Give the extent of all uninfected red blood cells.
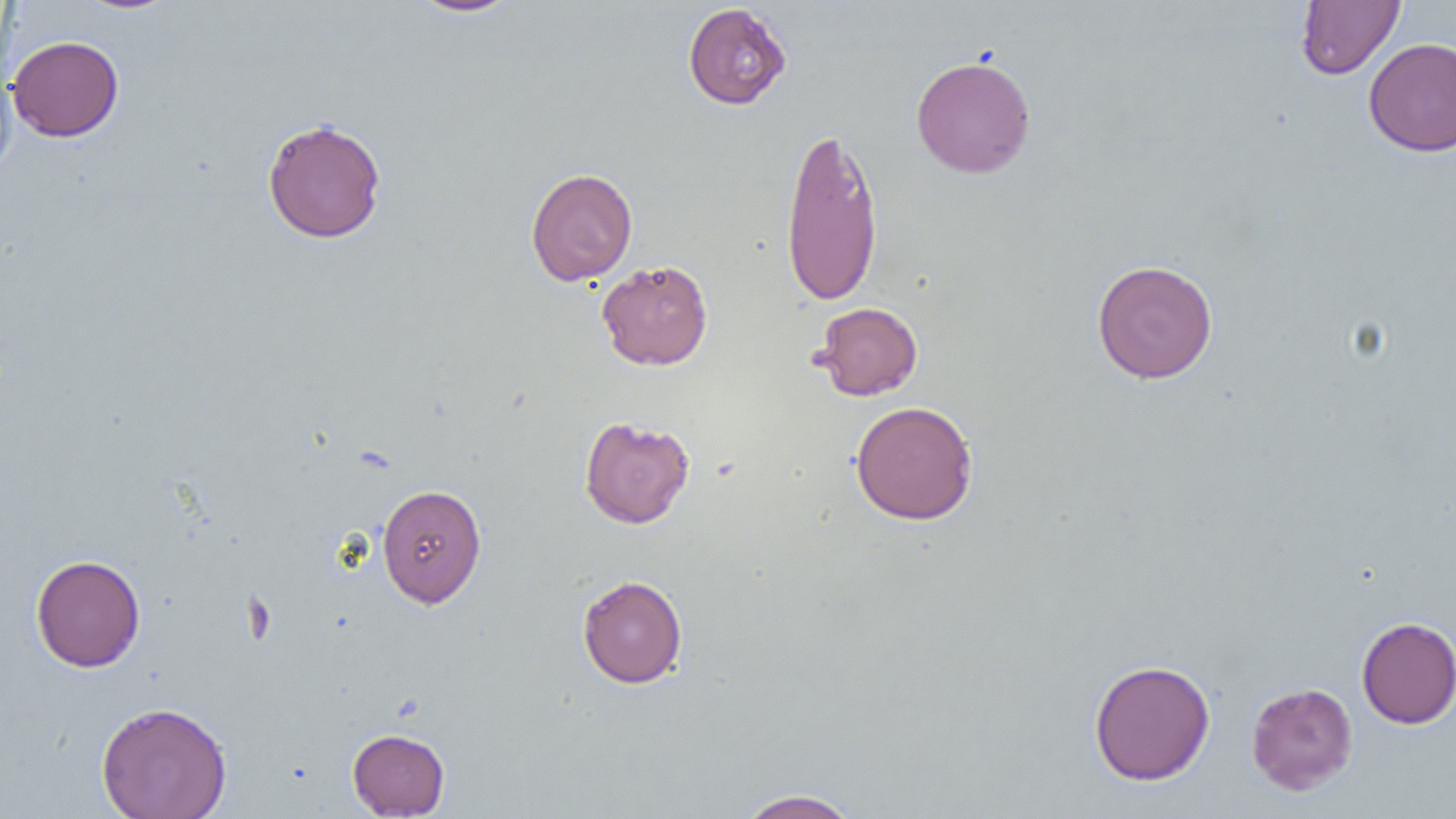
Approximate bounding boxes as named x1/y1/x2/y2 corners in pixels.
Uninfected red blood cells: (x1=76, y1=0, x2=181, y2=15), (x1=408, y1=0, x2=522, y2=17), (x1=1295, y1=1, x2=1406, y2=79), (x1=682, y1=3, x2=792, y2=110), (x1=7, y1=35, x2=124, y2=142), (x1=1363, y1=37, x2=1456, y2=156), (x1=910, y1=54, x2=1036, y2=179), (x1=0, y1=66, x2=18, y2=181), (x1=262, y1=117, x2=387, y2=244), (x1=779, y1=123, x2=884, y2=307), (x1=526, y1=167, x2=638, y2=286), (x1=596, y1=259, x2=713, y2=371), (x1=1092, y1=259, x2=1218, y2=384), (x1=814, y1=302, x2=923, y2=400), (x1=850, y1=400, x2=978, y2=525), (x1=579, y1=415, x2=695, y2=528), (x1=377, y1=483, x2=486, y2=608), (x1=30, y1=554, x2=145, y2=672), (x1=577, y1=574, x2=687, y2=688), (x1=1356, y1=616, x2=1456, y2=729), (x1=1088, y1=659, x2=1215, y2=785), (x1=1246, y1=682, x2=1358, y2=795), (x1=96, y1=701, x2=232, y2=819), (x1=347, y1=728, x2=450, y2=817), (x1=737, y1=788, x2=861, y2=818).

slide-level diagnosis = negative for blood parasites
preparation = thin blood film
image size = 1456×819 pixels
magnification = 1000x
field of view = single
modality = optical microscopy